State which cell type is depicted.
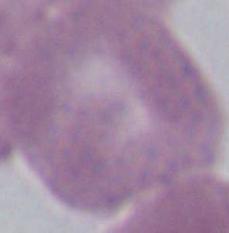

An erythrocyte.

1000x magnification. Micrograph.